Name the cell type shown.
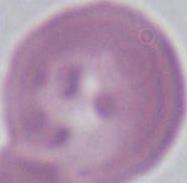
This is an erythrocyte.

Summary:
  - Modality: micrograph
  - Magnification: 1000x